Assess this cell for malaria.
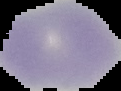
It is uninfected.

preparation = thin blood smear
image size = 121×91 pixels
image type = cell region segmented out of the field of view; surrounding area masked to black